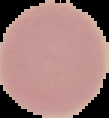

preparation = thin blood smear
image size = 109×118 pixels
image type = segmented cell region on a black background
malaria status = uninfected